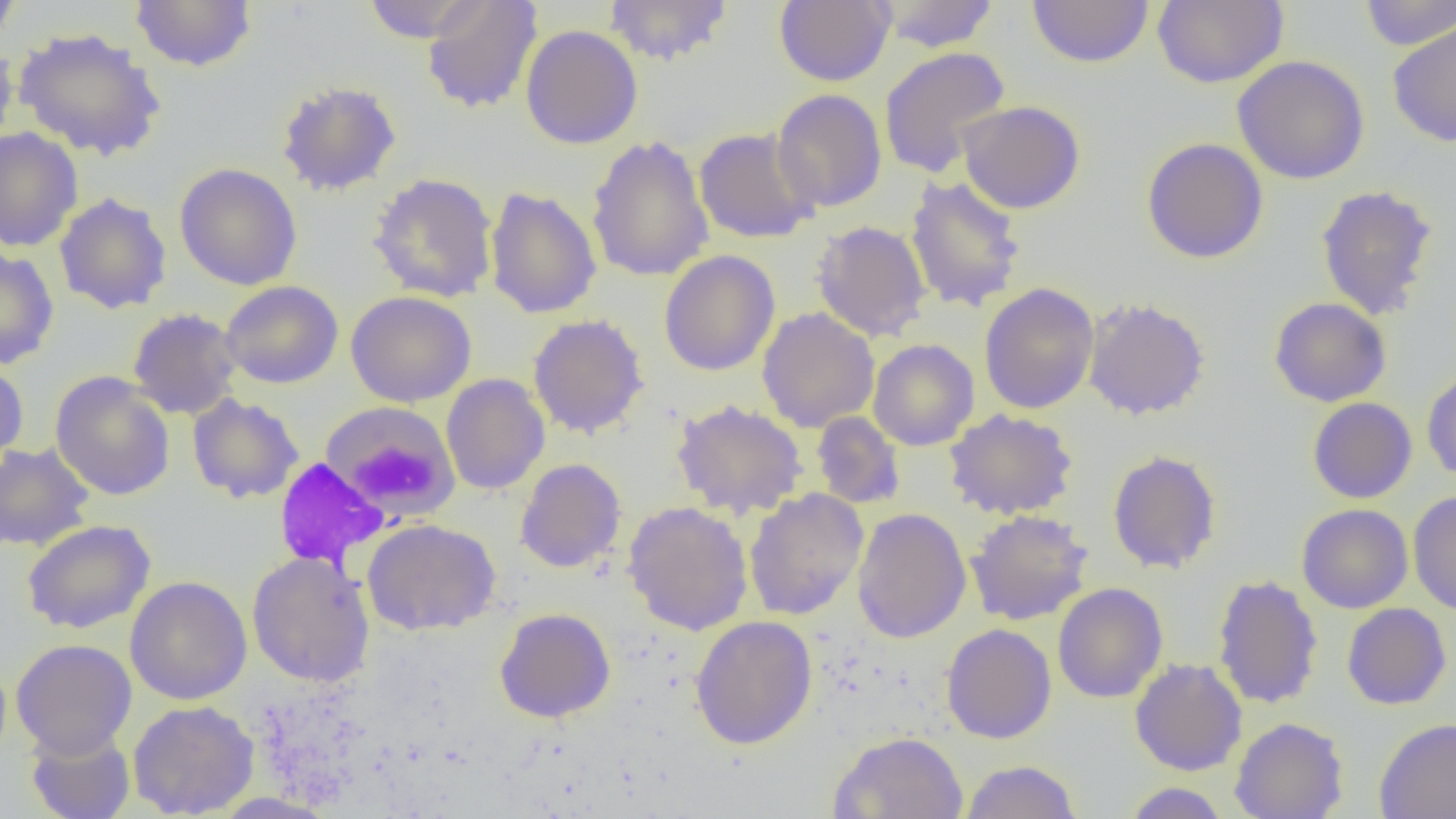
Approximate bounding boxes as named x1/y1/x2/y2 corners in pixels. Uninfected red blood cell locations: (x1=0, y1=0, x2=23, y2=46), (x1=129, y1=0, x2=257, y2=72), (x1=361, y1=0, x2=487, y2=43), (x1=422, y1=0, x2=543, y2=114), (x1=604, y1=0, x2=733, y2=66), (x1=774, y1=0, x2=895, y2=86), (x1=874, y1=0, x2=1000, y2=52), (x1=1027, y1=0, x2=1154, y2=68), (x1=1152, y1=0, x2=1288, y2=89), (x1=1358, y1=0, x2=1456, y2=50), (x1=1387, y1=19, x2=1456, y2=149), (x1=520, y1=25, x2=643, y2=149), (x1=13, y1=27, x2=166, y2=161), (x1=0, y1=41, x2=19, y2=153), (x1=878, y1=46, x2=1011, y2=179), (x1=1232, y1=55, x2=1370, y2=185), (x1=276, y1=80, x2=402, y2=197), (x1=771, y1=88, x2=888, y2=213), (x1=957, y1=101, x2=1085, y2=214), (x1=0, y1=127, x2=83, y2=252), (x1=694, y1=127, x2=820, y2=243), (x1=586, y1=135, x2=714, y2=283), (x1=1141, y1=138, x2=1269, y2=264), (x1=174, y1=162, x2=302, y2=291), (x1=368, y1=172, x2=499, y2=303), (x1=905, y1=175, x2=1027, y2=313), (x1=1315, y1=184, x2=1439, y2=319), (x1=485, y1=186, x2=601, y2=320), (x1=54, y1=193, x2=172, y2=315), (x1=812, y1=220, x2=931, y2=341), (x1=0, y1=247, x2=59, y2=370), (x1=659, y1=250, x2=780, y2=376), (x1=220, y1=280, x2=343, y2=389), (x1=978, y1=283, x2=1099, y2=414), (x1=346, y1=290, x2=476, y2=407), (x1=1082, y1=297, x2=1211, y2=421), (x1=1268, y1=297, x2=1391, y2=407), (x1=756, y1=307, x2=880, y2=432), (x1=127, y1=308, x2=243, y2=420), (x1=528, y1=314, x2=649, y2=439), (x1=868, y1=339, x2=979, y2=451), (x1=0, y1=360, x2=29, y2=473), (x1=1422, y1=368, x2=1456, y2=483), (x1=50, y1=372, x2=175, y2=500), (x1=441, y1=374, x2=550, y2=495), (x1=187, y1=394, x2=304, y2=503), (x1=1307, y1=397, x2=1417, y2=504), (x1=671, y1=399, x2=808, y2=519), (x1=319, y1=401, x2=461, y2=522), (x1=944, y1=408, x2=1079, y2=520), (x1=811, y1=411, x2=906, y2=509), (x1=0, y1=441, x2=94, y2=551), (x1=1107, y1=449, x2=1222, y2=575), (x1=515, y1=458, x2=626, y2=573), (x1=743, y1=488, x2=869, y2=621), (x1=1408, y1=491, x2=1456, y2=616), (x1=623, y1=500, x2=753, y2=636), (x1=1297, y1=504, x2=1413, y2=613), (x1=851, y1=508, x2=971, y2=644), (x1=965, y1=509, x2=1094, y2=626), (x1=362, y1=518, x2=501, y2=636), (x1=22, y1=519, x2=156, y2=634), (x1=247, y1=551, x2=375, y2=687), (x1=1211, y1=574, x2=1324, y2=710), (x1=125, y1=576, x2=252, y2=705), (x1=1052, y1=582, x2=1168, y2=703), (x1=1341, y1=602, x2=1452, y2=710), (x1=494, y1=608, x2=616, y2=723), (x1=690, y1=615, x2=818, y2=749), (x1=941, y1=623, x2=1057, y2=744), (x1=11, y1=638, x2=137, y2=759), (x1=1130, y1=658, x2=1247, y2=776), (x1=128, y1=699, x2=260, y2=818), (x1=1229, y1=717, x2=1348, y2=819), (x1=1374, y1=717, x2=1456, y2=819), (x1=25, y1=727, x2=136, y2=819), (x1=829, y1=731, x2=969, y2=819), (x1=961, y1=759, x2=1082, y2=819), (x1=1123, y1=782, x2=1230, y2=818). Slide-level diagnosis: negative for blood parasites. Image is 1456×819 pixels. Optical microscopy. Thin blood film. 1000x magnification. One field of a larger specimen.